Report the malaria status of this cell.
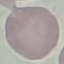
Uninfected.

{
  "stain": "Giemsa",
  "preparation": "thin smear",
  "capture": "smartphone through the microscope eyepiece",
  "image_type": "automatically extracted cell patch, resized to 64 × 64 pixels"
}